Name the parasite shown.
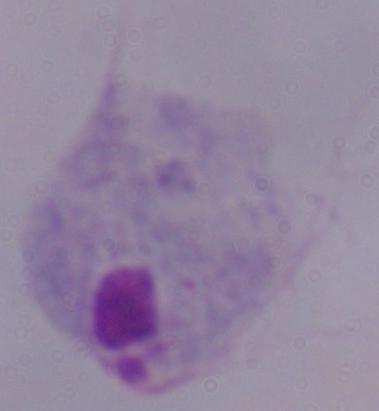

A trichomonad.

Photomicrograph. Captured at 1000x magnification.